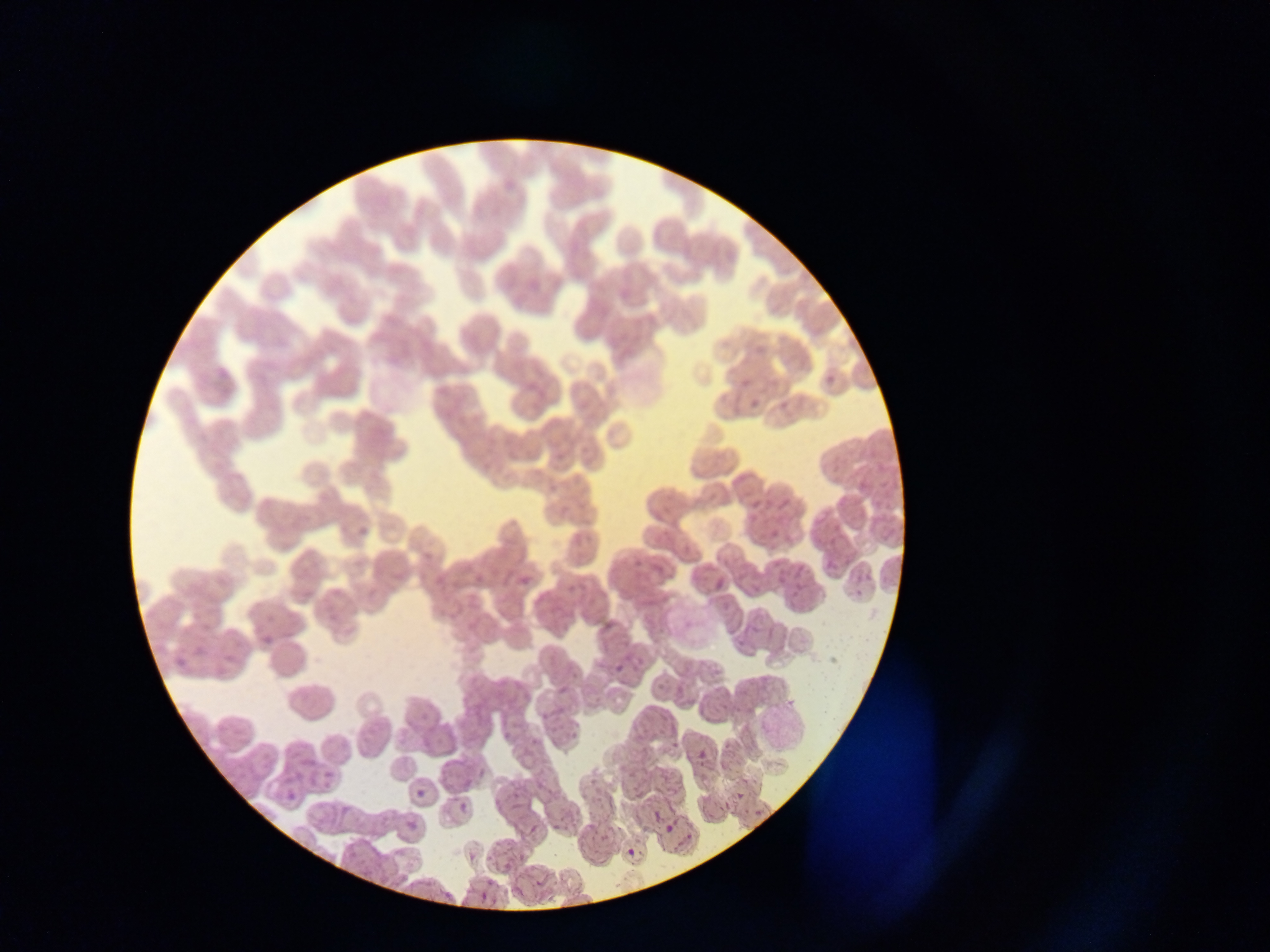 Approximate bounding boxes as [left, top, right, bottom] in pixels. Malaria parasite locations: [821, 371, 837, 388], [354, 517, 378, 538], [516, 576, 536, 591], [712, 580, 724, 594], [262, 635, 278, 646], [609, 659, 636, 675], [693, 739, 718, 764], [475, 764, 488, 781], [316, 765, 336, 785], [283, 786, 301, 811], [732, 786, 748, 803], [414, 789, 425, 798], [457, 800, 471, 817], [650, 809, 661, 824], [525, 819, 546, 843], [402, 820, 416, 841], [660, 820, 678, 838], [625, 841, 641, 858], [432, 887, 447, 902], [478, 891, 490, 908]. Thin blood film. One field of view. Image is 1270×952 pixels. Sample from Ghana. Mobile-phone photograph taken through the microscope.